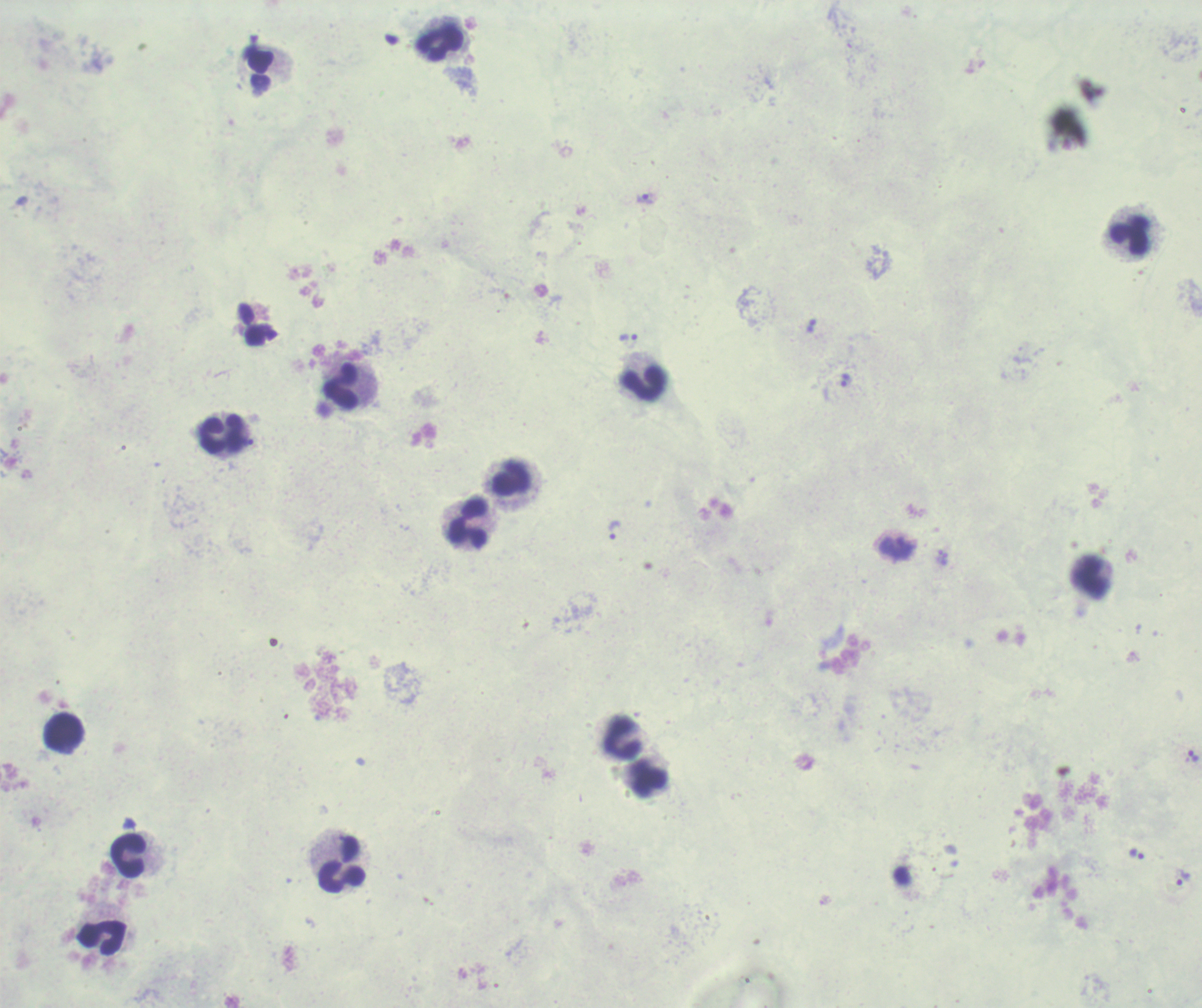

Approximate object centers, in pixels from the top-left corner.
Summary:
  - Leukocyte locations: (x=439, y=44), (x=1128, y=236), (x=643, y=383), (x=342, y=386), (x=222, y=435), (x=510, y=477), (x=467, y=523), (x=1092, y=578), (x=64, y=731), (x=621, y=735), (x=647, y=779), (x=128, y=855), (x=341, y=864), (x=102, y=937)
  - Trophozoite locations: (x=645, y=199), (x=810, y=327), (x=628, y=340), (x=845, y=381), (x=615, y=530), (x=896, y=547), (x=1194, y=755), (x=1137, y=853), (x=1183, y=877)
  - Magnification: 100x
  - Field of view: one from this slide
  - Stain: Romanowsky
  - Context: previously used in a real diagnosis
  - Result: malaria parasites identified
  - Image size: 1202×1008 pixels
  - Preparation: thick blood film
  - Background quality: unsatisfactory